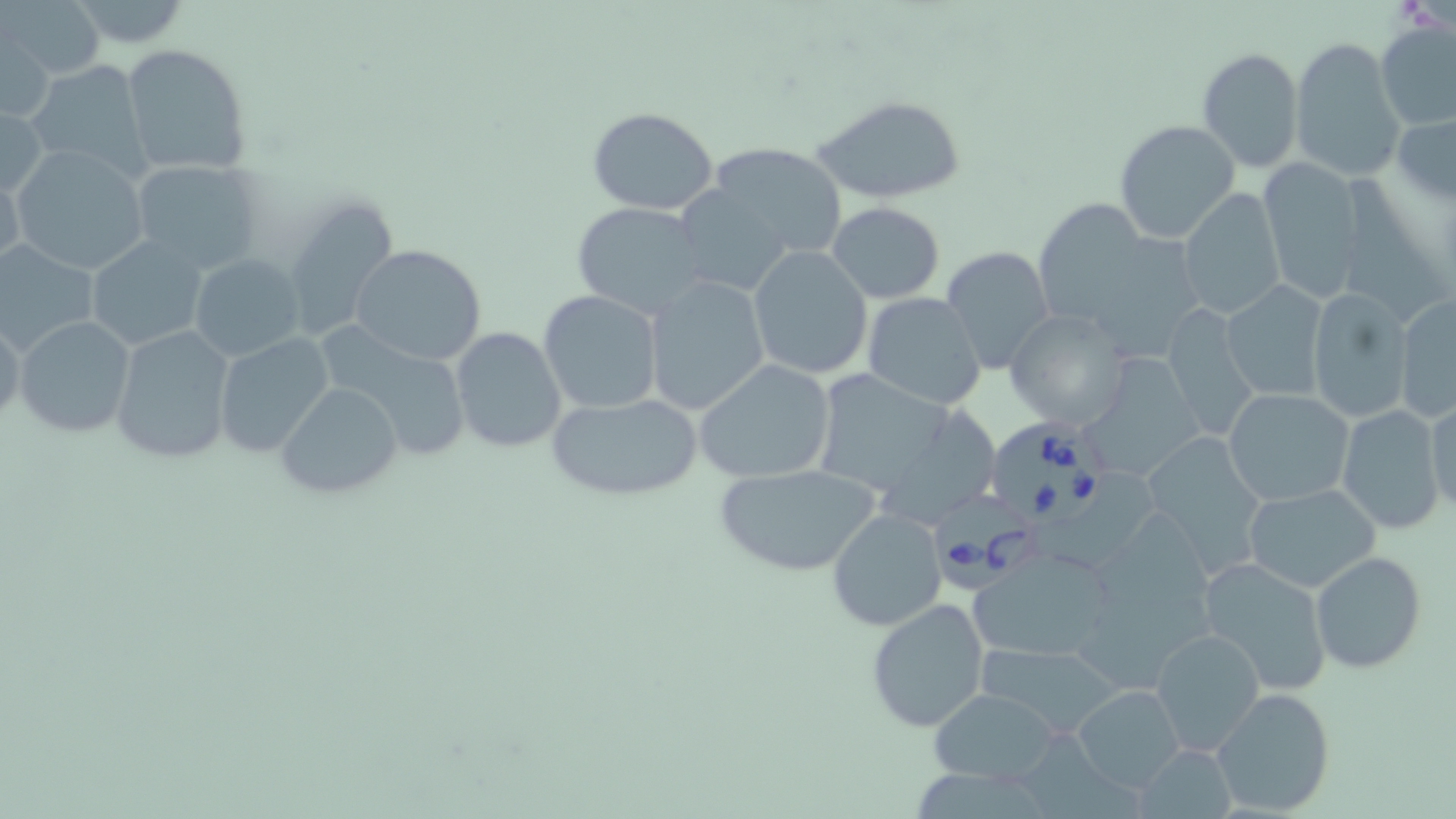

slide-level diagnosis = Babesia divergens
magnification = 1000x
field of view = one of a larger specimen
image size = 1456×819 pixels
Babesia divergens-infected red blood cell locations = approximate bounding boxes as [x1, y1, x2, y2] in pixels: [988, 421, 1110, 535], [934, 487, 1047, 589]
stain = May-Grünwald-Giemsa
modality = light microscopy
uninfected red blood cell locations = approximate bounding boxes as [x1, y1, x2, y2] in pixels: [57, 0, 196, 48], [5, 1, 104, 83], [1374, 20, 1455, 131], [1, 22, 55, 121], [1290, 36, 1407, 184], [121, 43, 254, 177], [1197, 46, 1304, 172], [24, 57, 154, 180], [814, 95, 966, 203], [0, 101, 49, 201], [587, 107, 720, 215], [1392, 109, 1456, 207], [1113, 120, 1241, 246], [702, 139, 849, 260], [9, 144, 151, 275], [1257, 158, 1369, 303], [130, 159, 266, 273], [0, 160, 25, 276], [673, 185, 793, 297], [1178, 187, 1287, 318], [279, 191, 401, 344], [1031, 195, 1170, 340], [571, 201, 712, 320], [828, 201, 946, 303], [88, 235, 208, 351], [0, 240, 100, 358], [349, 243, 486, 367], [748, 245, 872, 380], [940, 246, 1055, 375], [190, 255, 303, 360], [642, 276, 771, 416], [1222, 278, 1328, 402], [538, 290, 663, 415], [1305, 290, 1413, 424], [861, 292, 987, 411], [1393, 293, 1455, 425], [1160, 302, 1261, 443], [1004, 309, 1133, 431], [0, 313, 24, 430], [13, 314, 136, 438], [109, 323, 235, 465], [449, 327, 568, 453], [320, 331, 474, 463], [214, 333, 335, 457], [1090, 350, 1213, 486], [695, 359, 837, 483], [811, 370, 958, 497], [280, 382, 402, 499], [1224, 387, 1355, 506], [548, 392, 704, 502], [1423, 392, 1456, 518], [1335, 405, 1446, 534], [870, 408, 1001, 532], [1143, 429, 1271, 583], [715, 464, 879, 576], [1031, 473, 1158, 567], [1243, 482, 1381, 593], [826, 507, 948, 630], [970, 546, 1117, 664], [1310, 551, 1427, 675], [1195, 557, 1334, 698], [866, 597, 991, 732], [1150, 627, 1266, 756], [974, 640, 1118, 738], [1073, 685, 1186, 794], [1210, 686, 1337, 817], [927, 688, 1063, 785], [1019, 733, 1143, 819], [1134, 743, 1238, 818], [917, 765, 1047, 819]
preparation = thin blood smear